Assess this cell for malaria.
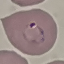

It is parasitized.

Summary:
  - Capture: smartphone through the microscope eyepiece
  - Preparation: thin smear
  - Image type: automatically extracted cell patch, resized to 64 × 64 pixels
  - Stain: Giemsa